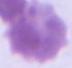

Summary:
  - Magnification: 1000x
  - Modality: micrograph
  - Identification: erythrocyte